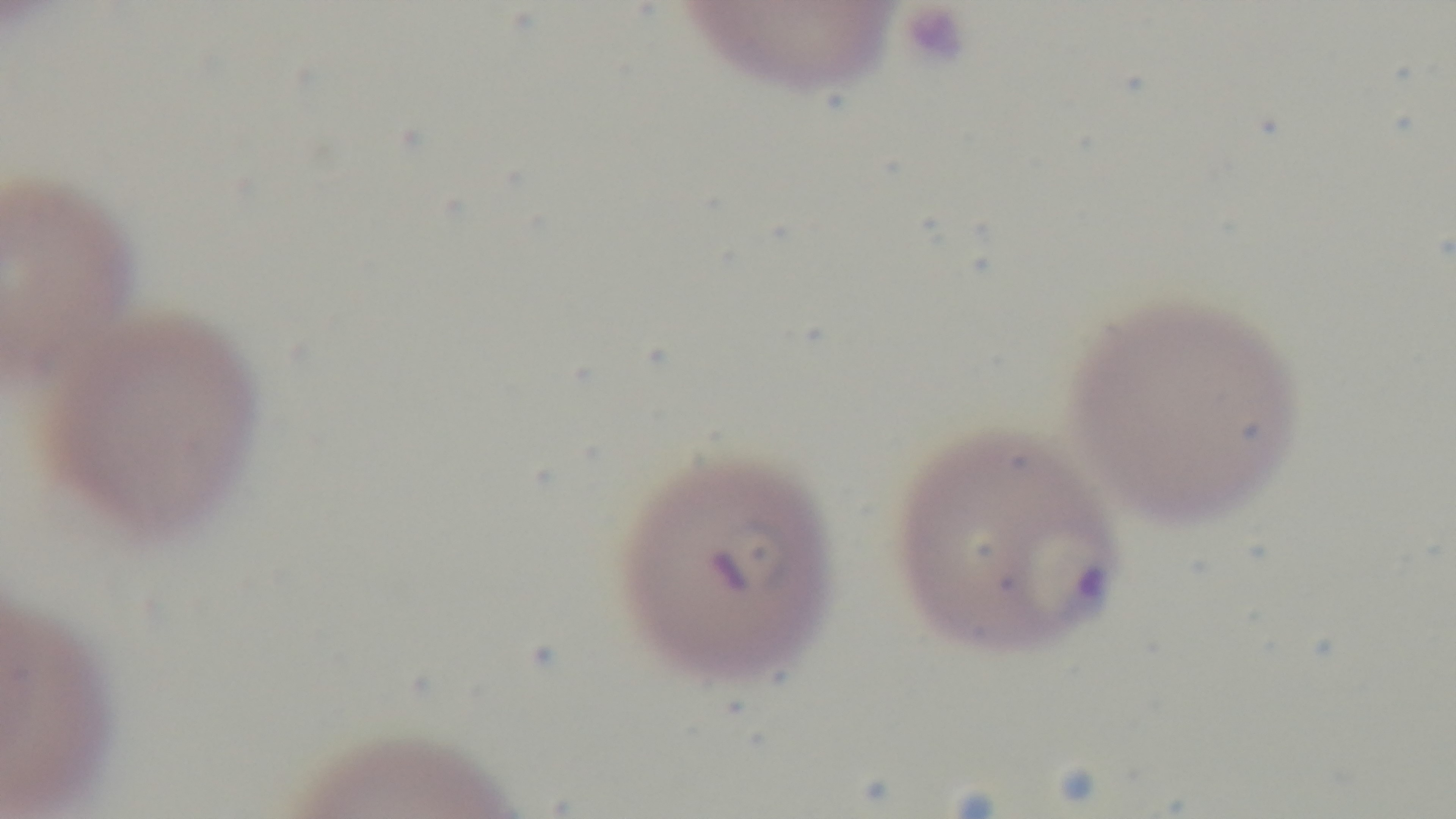
Summary:
  - Field of view: single
  - Stain: Giemsa
  - Objective: 100x oil immersion
  - Capture: mounted 4K digital camera
  - Modality: light microscopy
  - Preparation: thin blood film
  - Malaria status: infected